Assess the morphology of the red blood cells.
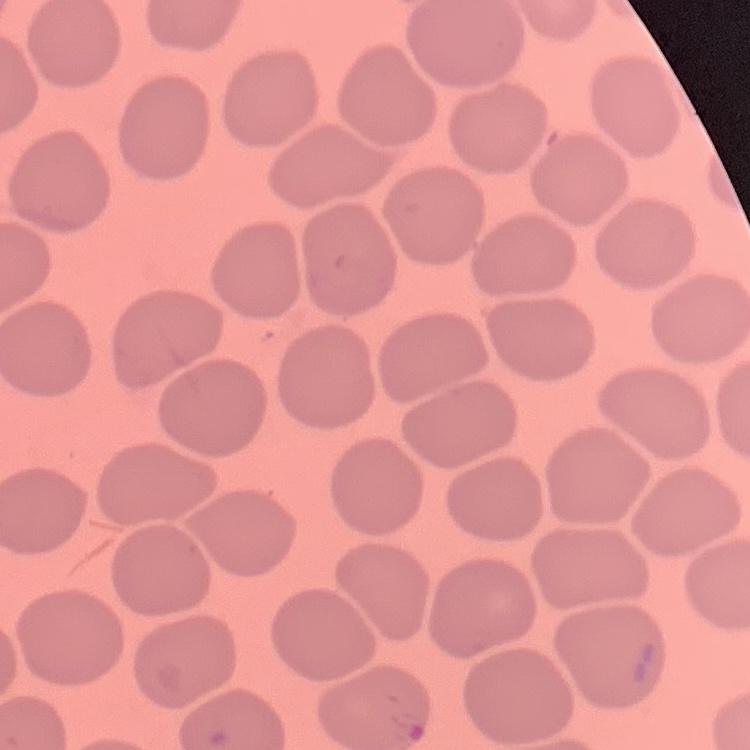

No rouleaux formation.

Field's or Giemsa stain. One tile cut from a larger photomicrograph. Thin blood smear.